Assess the morphology of the red blood cells.
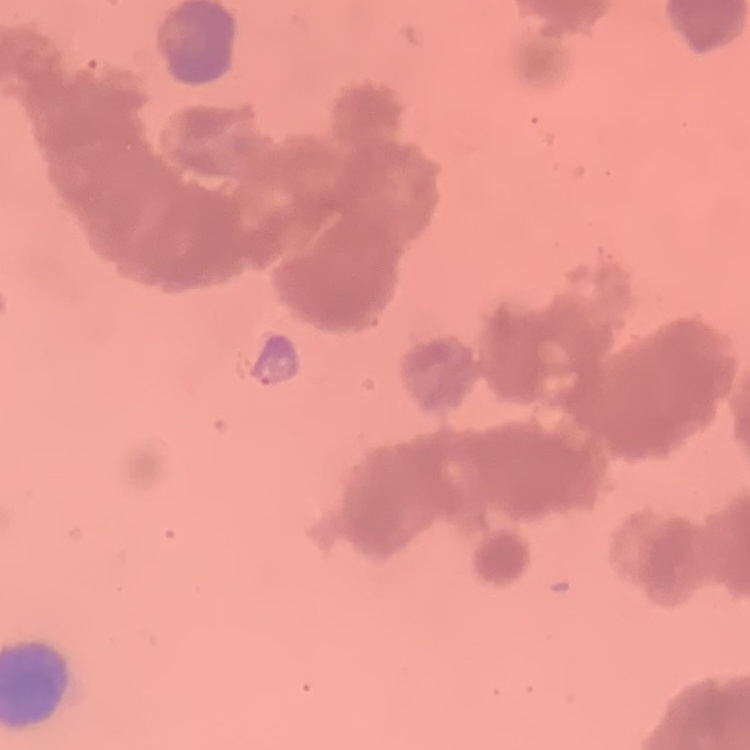
They show rouleaux formation.

Square crop of a larger photomicrograph. Thin peripheral smear. Field's or Giemsa stain.